Assess this cell for malaria.
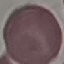

It is uninfected.

image_type: automatically extracted cell patch, resized to 64 × 64 pixels
preparation: thin blood film
capture: smartphone camera at the microscope eyepiece
stain: Giemsa